Locate every Plasmodium falciparum-infected red blood cell.
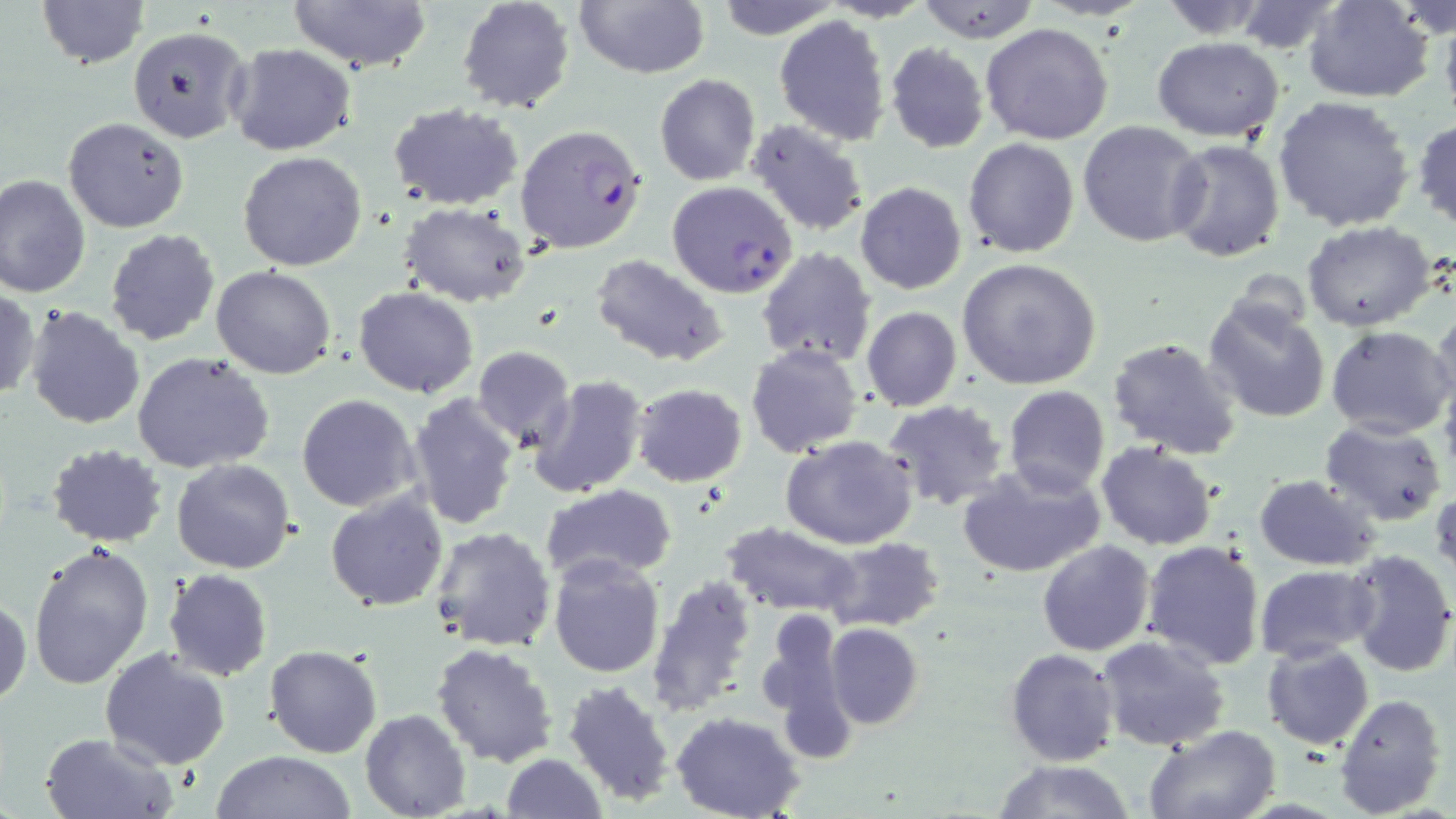

Approximate bounding boxes as named x1/y1/x2/y2 corners in pixels.
Plasmodium falciparum-infected red blood cells: (x1=514, y1=122, x2=647, y2=255), (x1=667, y1=181, x2=798, y2=299).

slide-level diagnosis = Plasmodium falciparum
magnification = 1000x
image size = 1456×819 pixels
preparation = thin blood film
field of view = one of a larger specimen
modality = light microscopy
uninfected red blood cell locations = approximate bounding boxes as named x1/y1/x2/y2 corners in pixels: (x1=38, y1=0, x2=147, y2=69), (x1=286, y1=0, x2=434, y2=72), (x1=457, y1=0, x2=576, y2=115), (x1=714, y1=0, x2=846, y2=40), (x1=913, y1=0, x2=1042, y2=43), (x1=1153, y1=0, x2=1275, y2=38), (x1=1303, y1=0, x2=1434, y2=102), (x1=574, y1=1, x2=710, y2=79), (x1=1229, y1=1, x2=1350, y2=55), (x1=1439, y1=5, x2=1456, y2=126), (x1=774, y1=14, x2=890, y2=145), (x1=980, y1=23, x2=1114, y2=146), (x1=126, y1=25, x2=250, y2=143), (x1=1153, y1=37, x2=1284, y2=141), (x1=225, y1=42, x2=357, y2=157), (x1=885, y1=42, x2=990, y2=153), (x1=654, y1=74, x2=760, y2=185), (x1=1274, y1=94, x2=1416, y2=232), (x1=387, y1=102, x2=523, y2=208), (x1=63, y1=116, x2=189, y2=233), (x1=1411, y1=117, x2=1456, y2=233), (x1=747, y1=118, x2=871, y2=236), (x1=1077, y1=120, x2=1207, y2=247), (x1=964, y1=137, x2=1079, y2=257), (x1=1166, y1=139, x2=1285, y2=262), (x1=238, y1=151, x2=367, y2=272), (x1=0, y1=174, x2=91, y2=298), (x1=856, y1=182, x2=966, y2=294), (x1=400, y1=202, x2=532, y2=307), (x1=1302, y1=221, x2=1439, y2=332), (x1=105, y1=229, x2=220, y2=346), (x1=755, y1=249, x2=876, y2=367), (x1=591, y1=255, x2=731, y2=368), (x1=956, y1=258, x2=1103, y2=390), (x1=211, y1=265, x2=336, y2=380), (x1=355, y1=286, x2=479, y2=398), (x1=1, y1=287, x2=40, y2=402), (x1=1203, y1=298, x2=1331, y2=423), (x1=24, y1=306, x2=145, y2=430), (x1=861, y1=306, x2=961, y2=412), (x1=1432, y1=307, x2=1456, y2=415), (x1=1326, y1=325, x2=1455, y2=439), (x1=1108, y1=337, x2=1241, y2=460), (x1=746, y1=343, x2=864, y2=460), (x1=471, y1=345, x2=575, y2=452), (x1=132, y1=352, x2=275, y2=474), (x1=528, y1=375, x2=650, y2=500), (x1=632, y1=384, x2=746, y2=487), (x1=1003, y1=386, x2=1110, y2=497), (x1=296, y1=394, x2=420, y2=512), (x1=407, y1=394, x2=519, y2=529), (x1=882, y1=400, x2=1009, y2=515), (x1=1320, y1=418, x2=1448, y2=526), (x1=782, y1=436, x2=918, y2=550), (x1=45, y1=442, x2=169, y2=548), (x1=1096, y1=442, x2=1218, y2=550), (x1=170, y1=458, x2=296, y2=574), (x1=956, y1=461, x2=1107, y2=579), (x1=1254, y1=475, x2=1383, y2=570), (x1=542, y1=483, x2=678, y2=581), (x1=1431, y1=484, x2=1455, y2=586), (x1=325, y1=491, x2=449, y2=612), (x1=721, y1=520, x2=863, y2=619), (x1=428, y1=526, x2=558, y2=651), (x1=824, y1=538, x2=944, y2=630), (x1=1142, y1=538, x2=1266, y2=671), (x1=1037, y1=539, x2=1155, y2=657), (x1=27, y1=542, x2=155, y2=692), (x1=1345, y1=549, x2=1456, y2=677), (x1=548, y1=553, x2=666, y2=677), (x1=1253, y1=564, x2=1378, y2=662), (x1=164, y1=569, x2=272, y2=680), (x1=644, y1=577, x2=757, y2=718), (x1=0, y1=596, x2=30, y2=708), (x1=756, y1=611, x2=851, y2=735), (x1=824, y1=622, x2=923, y2=730), (x1=1095, y1=636, x2=1232, y2=753), (x1=431, y1=642, x2=559, y2=768), (x1=1261, y1=643, x2=1374, y2=748), (x1=264, y1=644, x2=382, y2=757), (x1=101, y1=647, x2=232, y2=769), (x1=1004, y1=648, x2=1119, y2=765), (x1=561, y1=678, x2=677, y2=807), (x1=1334, y1=692, x2=1447, y2=816), (x1=360, y1=709, x2=470, y2=819), (x1=671, y1=712, x2=804, y2=819), (x1=1144, y1=723, x2=1282, y2=819), (x1=40, y1=731, x2=176, y2=818), (x1=210, y1=750, x2=359, y2=819), (x1=500, y1=754, x2=607, y2=818), (x1=994, y1=760, x2=1136, y2=818)
stain = May-Grünwald-Giemsa